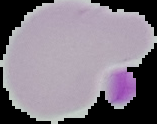

Summary:
  - Preparation: thin blood film
  - Result: no malaria parasites detected
  - Image size: 157×124 pixels
  - Image type: segmented cell region with the area outside set to black